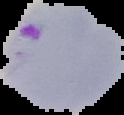

result = Plasmodium parasites identified
image type = segmented cell region with the area outside set to black
preparation = thin blood film
image size = 124×115 pixels